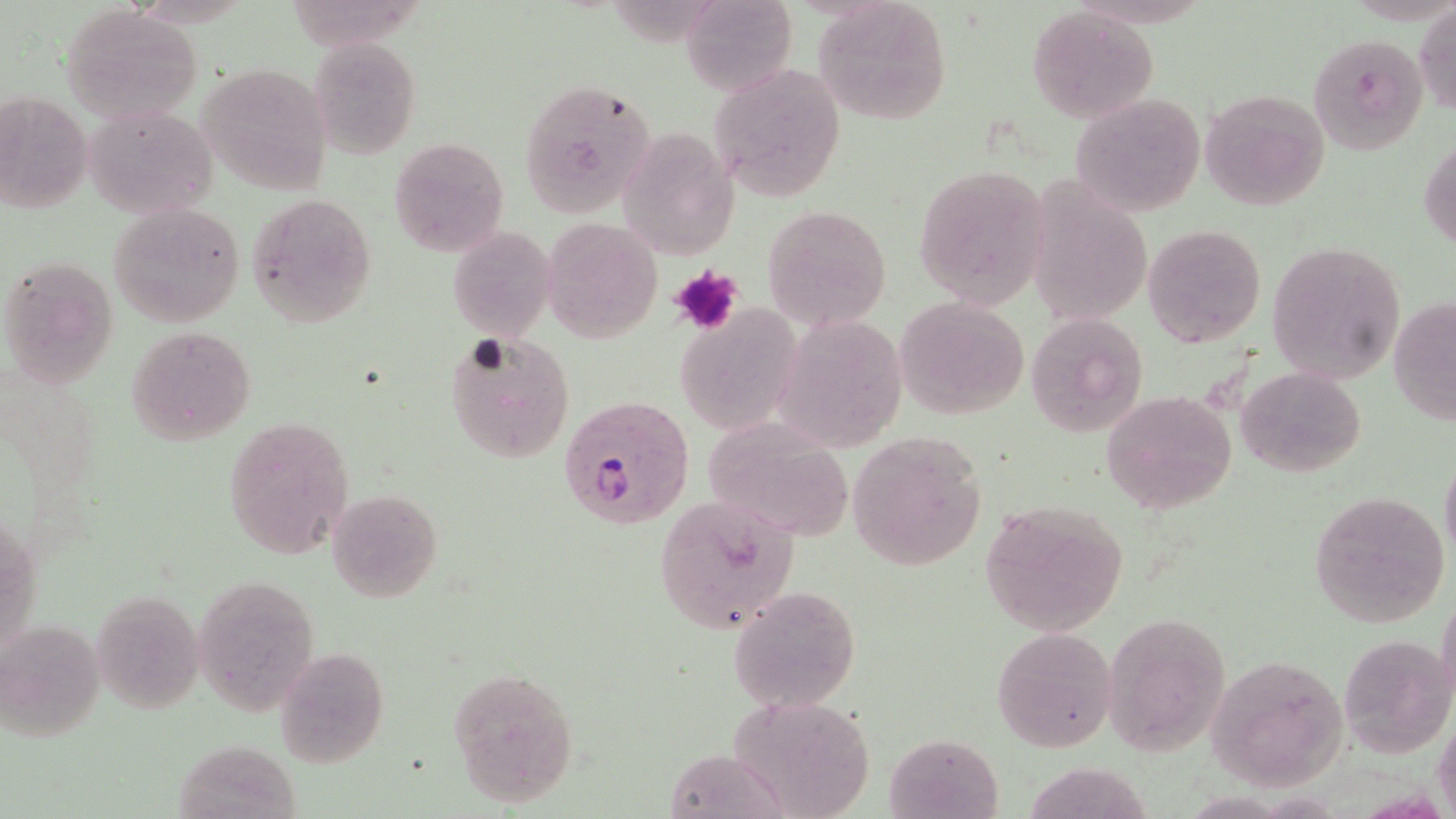
slide-level diagnosis = Plasmodium falciparum
stain = May-Grünwald-Giemsa
magnification = 1000x
field of view = single
uninfected red blood cell locations = approximate bounding boxes as (x1, y1, x2, y2) in pixels: (682, 1, 797, 98), (812, 1, 953, 126), (1414, 3, 1456, 118), (63, 7, 202, 121), (1028, 8, 1160, 122), (1310, 34, 1426, 153), (310, 37, 423, 157), (711, 62, 845, 197), (196, 63, 333, 195), (519, 78, 655, 216), (0, 89, 93, 215), (1199, 89, 1330, 209), (1069, 93, 1207, 218), (84, 104, 218, 220), (619, 125, 738, 262), (1420, 132, 1456, 255), (390, 137, 509, 256), (912, 164, 1052, 307), (246, 193, 377, 327), (107, 201, 246, 328), (763, 204, 891, 331), (543, 216, 663, 344), (1142, 223, 1267, 349), (446, 226, 556, 342), (1265, 242, 1404, 383), (0, 254, 119, 390), (895, 296, 1030, 421), (1389, 297, 1456, 425), (676, 302, 801, 436), (1023, 312, 1147, 438), (126, 326, 256, 445), (443, 332, 576, 464), (1234, 366, 1366, 477), (1101, 391, 1237, 513), (222, 417, 353, 558), (849, 431, 985, 568), (1439, 448, 1456, 563), (328, 489, 443, 604), (1308, 492, 1451, 627), (653, 496, 802, 635), (980, 500, 1129, 636), (194, 572, 323, 714), (726, 586, 861, 712), (92, 589, 205, 713), (1102, 610, 1235, 755), (992, 625, 1118, 753), (1337, 632, 1453, 758), (276, 648, 390, 768), (1207, 652, 1352, 789), (449, 668, 579, 808), (727, 695, 879, 819), (1434, 702, 1456, 819), (885, 733, 1003, 818), (1017, 765, 1154, 819)
modality = light microscopy
image size = 1456×819 pixels
platelet locations = approximate bounding boxes as (x1, y1, x2, y2) in pixels: (668, 263, 741, 335)
Plasmodium falciparum-infected red blood cell locations = approximate bounding boxes as (x1, y1, x2, y2) in pixels: (561, 396, 694, 532)
preparation = thin blood smear